Describe the morphology of the red blood cells.
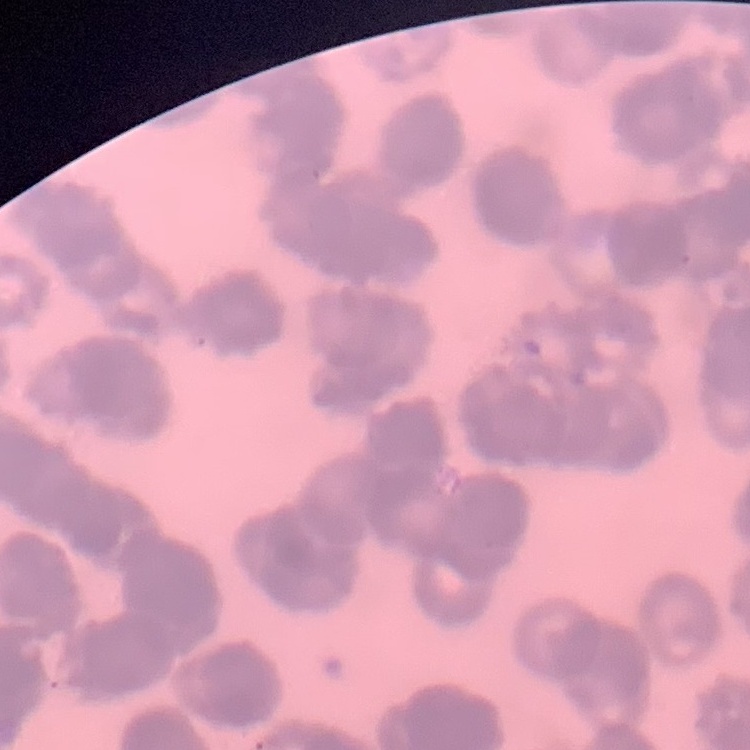
They show rouleaux formation.

stain: Field's or Giemsa
image_type: square crop of a larger photomicrograph
preparation: thin blood film